Point out each malaria parasite and each leukocyte.
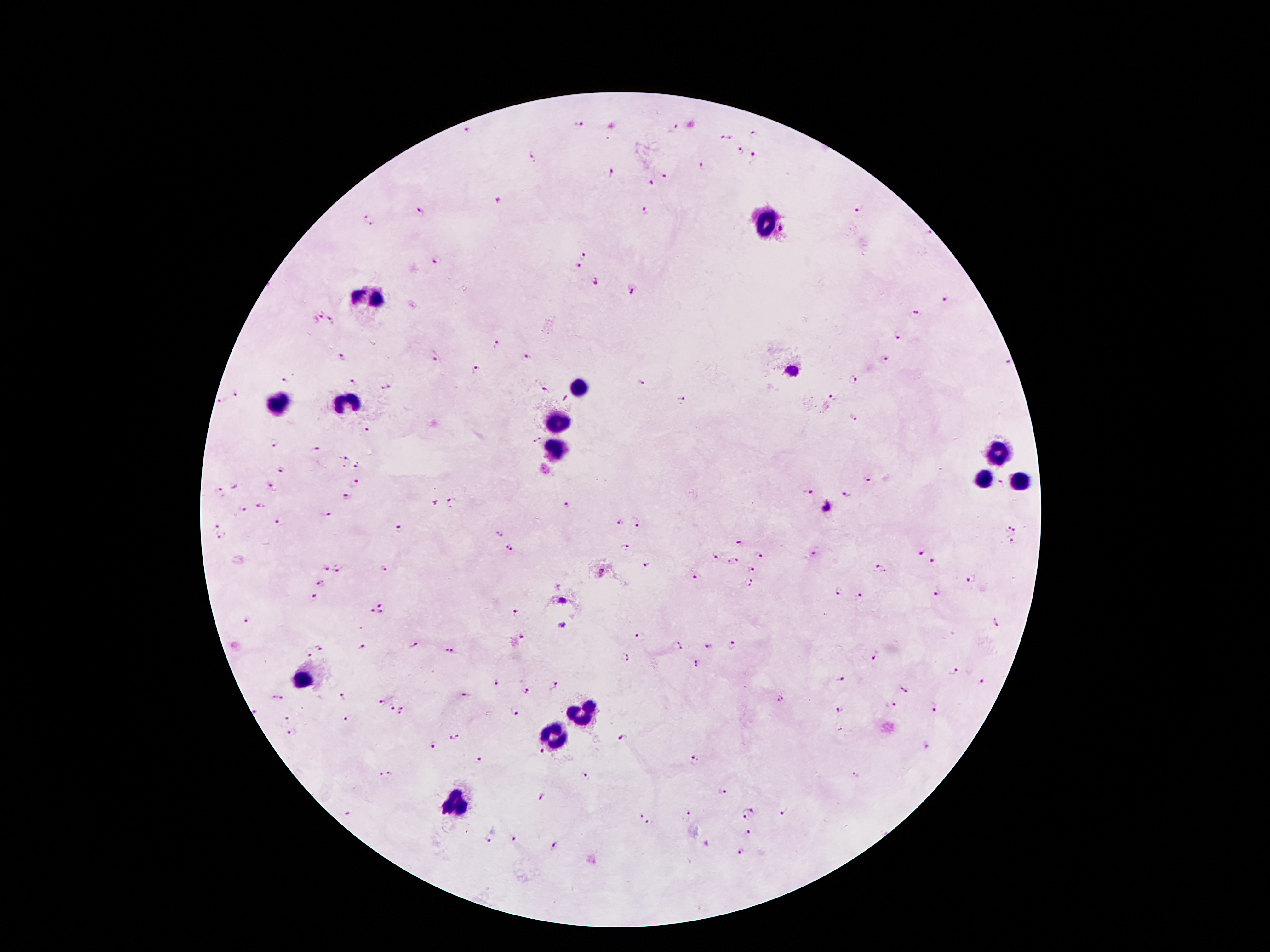

Approximate centers as {x, y} in pixels.
Malaria parasites: {578, 122}, {673, 128}, {466, 132}, {754, 134}, {722, 136}, {729, 137}, {740, 150}, {532, 157}, {754, 160}, {701, 167}, {612, 173}, {665, 176}, {649, 183}, {498, 202}, {859, 208}, {645, 212}, {421, 213}, {368, 220}, {782, 230}, {928, 233}, {583, 254}, {438, 261}, {576, 265}, {597, 283}, {633, 290}, {946, 302}, {319, 310}, {915, 316}, {332, 321}, {899, 334}, {496, 345}, {436, 356}, {341, 357}, {525, 359}, {883, 359}, {1008, 361}, {475, 369}, {792, 372}, {283, 380}, {852, 380}, {352, 382}, {642, 382}, {385, 387}, {542, 388}, {235, 392}, {832, 397}, {219, 400}, {683, 400}, {854, 418}, {367, 429}, {536, 440}, {272, 442}, {315, 449}, {346, 459}, {358, 468}, {283, 470}, {869, 477}, {356, 484}, {234, 485}, {269, 486}, {220, 492}, {807, 492}, {846, 495}, {348, 498}, {452, 502}, {434, 503}, {565, 506}, {827, 506}, {262, 507}, {243, 508}, {326, 514}, {279, 524}, {618, 524}, {215, 525}, {637, 526}, {397, 527}, {1007, 530}, {1015, 531}, {498, 534}, {222, 538}, {737, 542}, {1011, 544}, {625, 546}, {509, 547}, {815, 553}, {922, 553}, {714, 556}, {758, 556}, {932, 559}, {731, 560}, {646, 566}, {749, 567}, {337, 568}, {880, 569}, {323, 570}, {386, 570}, {602, 573}, {694, 577}, {970, 581}, {749, 583}, {320, 584}, {557, 586}, {838, 593}, {938, 594}, {860, 595}, {312, 598}, {562, 601}, {379, 605}, {372, 611}, {381, 613}, {516, 613}, {247, 620}, {995, 622}, {563, 624}, {640, 635}, {523, 638}, {731, 644}, {415, 645}, {322, 646}, {674, 647}, {709, 648}, {362, 649}, {310, 651}, {449, 651}, {873, 655}, {624, 656}, {695, 664}, {954, 672}, {841, 677}, {983, 680}, {497, 684}, {553, 684}, {905, 689}, {527, 691}, {465, 696}, {272, 697}, {342, 697}, {283, 698}, {778, 701}, {381, 702}, {392, 706}, {891, 706}, {402, 707}, {933, 708}, {839, 710}, {515, 712}, {255, 713}, {398, 715}, {287, 717}, {347, 719}, {291, 732}, {454, 737}, {621, 738}, {433, 746}, {926, 747}, {541, 751}, {478, 760}, {696, 760}, {391, 772}, {382, 775}, {855, 775}, {584, 776}, {723, 792}, {540, 796}, {751, 808}, {347, 812}, {783, 812}, {687, 814}, {641, 816}, {745, 816}, {648, 823}, {749, 832}, {489, 838}, {514, 838}, {553, 845}, {707, 845}, {741, 852}.
Leukocytes: {767, 221}, {372, 297}, {579, 386}, {347, 405}, {281, 407}, {558, 422}, {552, 448}, {996, 456}, {982, 479}, {1017, 479}, {301, 682}, {582, 715}, {555, 732}, {453, 810}.

preparation: thick peripheral-blood smear
image_size: 1270×952 pixels
stain: Giemsa
field_of_view: one from this slide
capture: smartphone camera through the microscope eyepiece
patient_malaria_status: positive for Plasmodium falciparum
magnification: 100x